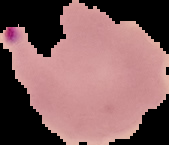

Summary:
  - Malaria status: parasitized
  - Image type: segmented cell region with the area outside set to black
  - Image size: 169×145 pixels
  - Preparation: thin blood smear